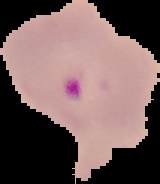
image size = 160×184 pixels
image type = segmented cell region with the area outside set to black
preparation = thin blood film
malaria status = parasitized